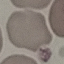

{
  "malaria_status": "uninfected",
  "capture": "smartphone through the microscope eyepiece",
  "stain": "Giemsa",
  "preparation": "thin blood film",
  "image_type": "automatically extracted cell patch, resized to 64 × 64 pixels"
}